Look for Plasmodium parasites.
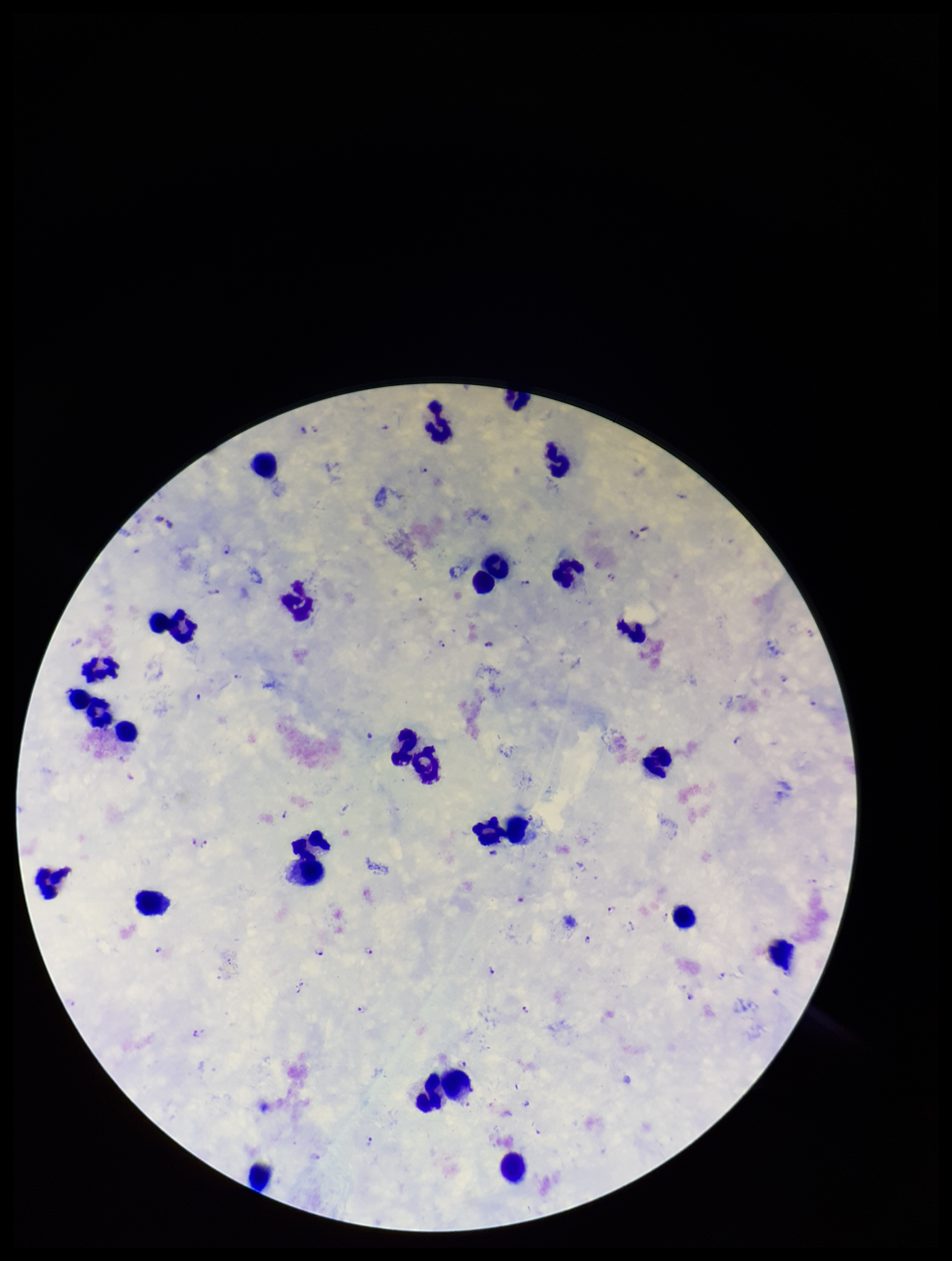
Seen.

Preparation: thick blood smear. Image is 952×1261 pixels. Giemsa stain. Leukocyte count: 26. Parasite count: 32. Smartphone photograph taken through the eyepiece of a microscope. One field from this slide. Species reported for this patient: Plasmodium falciparum. Patient malaria status: positive.